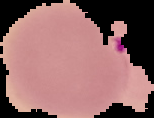
Summary:
  - Image size: 154×118 pixels
  - Malaria status: parasitized
  - Preparation: thin blood smear
  - Image type: cell region segmented out of the field of view; surrounding area masked to black